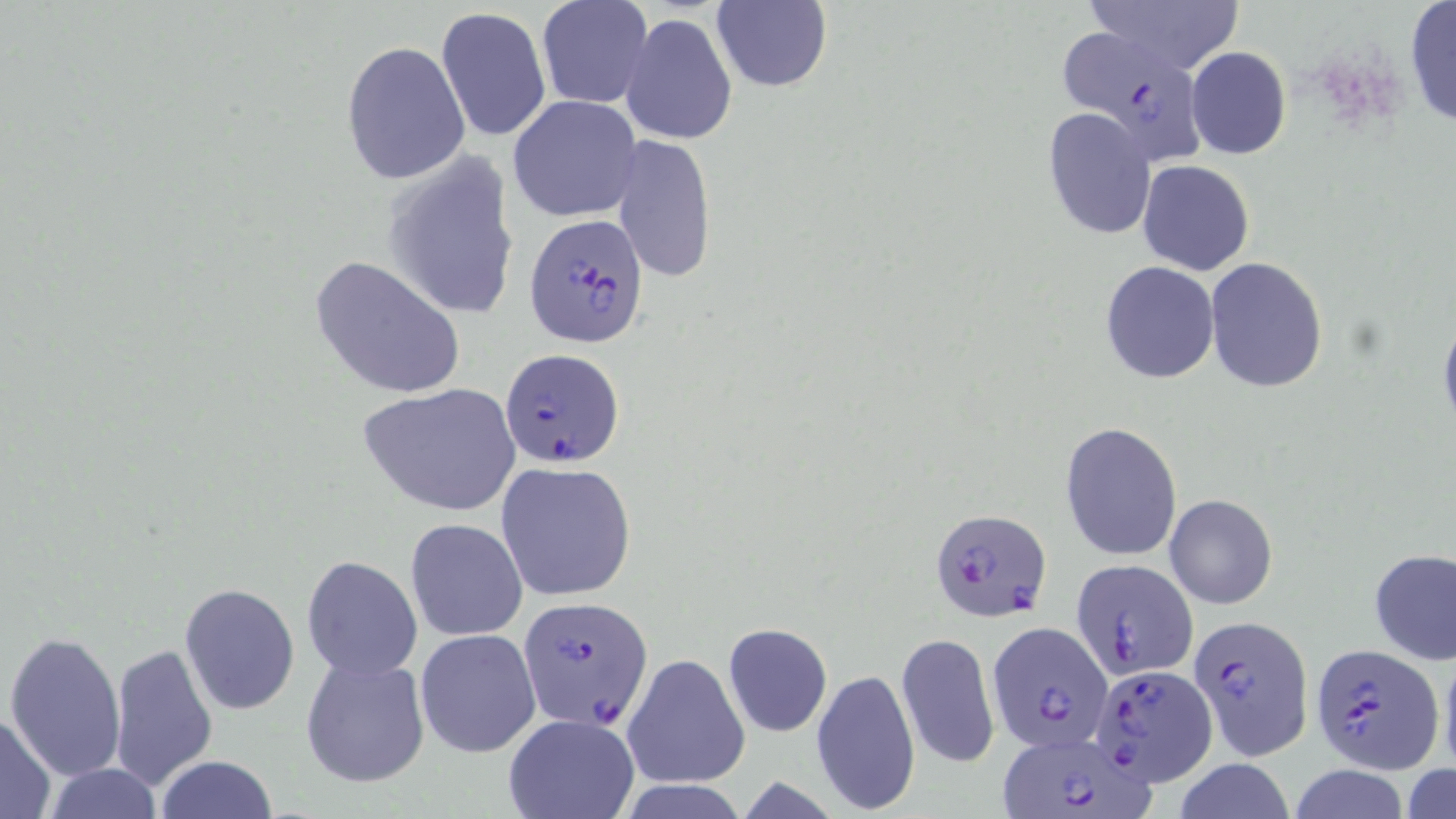

Approximate bounding boxes as [x1, y1, x2, y2] in pixels. Uninfected red blood cell locations: [1077, 0, 1246, 78], [534, 1, 650, 113], [710, 1, 832, 93], [1403, 1, 1455, 127], [436, 7, 551, 142], [620, 12, 738, 146], [340, 40, 470, 185], [1185, 47, 1291, 159], [508, 96, 641, 222], [1042, 107, 1156, 239], [611, 134, 718, 282], [380, 152, 522, 323], [1137, 159, 1254, 275], [309, 254, 468, 401], [1204, 257, 1329, 393], [1100, 262, 1220, 383], [1438, 308, 1456, 441], [358, 383, 521, 516], [1059, 420, 1184, 562], [496, 461, 637, 602], [1164, 493, 1278, 610], [405, 519, 526, 640], [1369, 548, 1456, 665], [300, 554, 423, 682], [179, 583, 300, 716], [722, 624, 833, 737], [415, 628, 542, 759], [6, 631, 126, 782], [896, 631, 1000, 769], [108, 642, 218, 793], [1438, 647, 1456, 781], [622, 653, 750, 791], [301, 655, 430, 789], [811, 669, 920, 812], [0, 710, 57, 819], [503, 714, 640, 819], [154, 755, 278, 819], [1170, 759, 1297, 819], [39, 764, 164, 819], [1402, 764, 1456, 819], [1287, 765, 1412, 819], [614, 781, 752, 819]. Plasmodium falciparum-infected red blood cell locations: [1058, 28, 1214, 161], [526, 213, 653, 350], [500, 347, 624, 466], [927, 506, 1052, 623], [1072, 558, 1197, 680], [520, 597, 653, 727], [1189, 614, 1315, 759], [985, 621, 1113, 753], [1311, 643, 1441, 772], [1085, 663, 1219, 785], [998, 731, 1153, 817]. Slide-level diagnosis: Plasmodium falciparum. Thin blood smear. Single field of view. Captured at 1000x magnification. Image is 1456×819 pixels. May-Grünwald-Giemsa stain. Light microscopy.